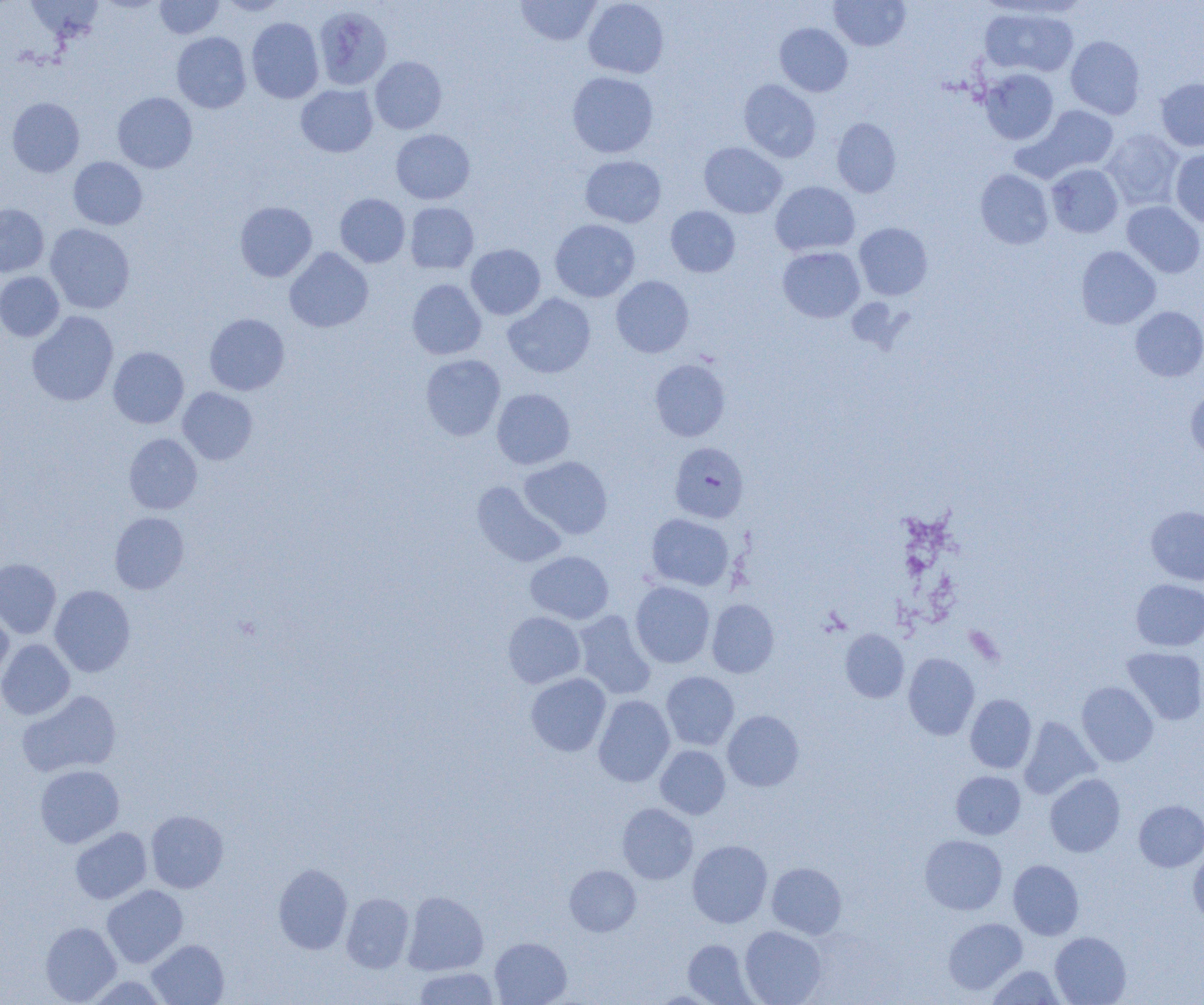
Summary:
  - Coordinate format: approximate bounding boxes as (x1,y1)-(x2,y2) corner pairs in pixels
  - Uninfected red blood cell locations: (26,0)-(103,43), (154,0)-(224,39), (218,0)-(289,16), (516,0)-(602,46), (583,0)-(669,78), (829,0)-(910,51), (314,6)-(392,91), (980,7)-(1079,77), (246,17)-(324,103), (775,23)-(853,96), (172,32)-(251,113), (1066,35)-(1145,119), (370,56)-(447,134), (980,69)-(1058,144), (567,72)-(658,158), (1155,77)-(1204,152), (739,80)-(821,162), (296,84)-(378,157), (112,92)-(197,173), (7,97)-(85,177), (1027,105)-(1119,177), (832,117)-(901,197), (391,129)-(475,204), (1102,129)-(1184,210), (698,142)-(786,218), (1170,149)-(1204,228), (580,155)-(666,227), (68,157)-(147,229), (1046,163)-(1123,238), (975,169)-(1053,249), (771,181)-(860,256), (335,193)-(410,267), (235,201)-(317,282), (1121,201)-(1204,278), (405,202)-(479,274), (0,203)-(49,277), (665,206)-(740,277), (550,219)-(640,302), (854,222)-(933,300), (45,224)-(135,314), (466,244)-(546,320), (1076,245)-(1161,330), (778,246)-(865,322), (284,247)-(373,332), (0,271)-(64,341), (611,275)-(694,357), (407,279)-(487,360), (503,293)-(596,378), (1130,306)-(1204,381), (26,311)-(119,406), (204,313)-(289,395), (108,346)-(189,428), (420,354)-(505,441), (650,359)-(730,441), (177,387)-(258,465), (492,388)-(575,469), (1185,389)-(1204,461), (124,433)-(202,514), (519,456)-(613,539), (471,481)-(567,567), (1146,505)-(1204,585), (109,512)-(189,594), (646,513)-(734,591), (525,551)-(614,624), (0,558)-(61,639), (1131,578)-(1204,651), (630,581)-(715,668), (49,585)-(136,676), (707,599)-(779,677), (0,608)-(13,686), (573,610)-(656,699), (503,611)-(585,688), (840,629)-(909,702), (0,639)-(75,719), (1121,647)-(1204,725), (903,653)-(979,739), (661,671)-(740,750), (526,673)-(611,756), (1076,681)-(1158,766), (18,689)-(122,777), (965,694)-(1037,773), (593,695)-(675,787), (722,710)-(804,791), (1019,717)-(1100,799), (655,745)-(730,819), (34,764)-(124,848), (951,771)-(1025,839), (1045,774)-(1125,857), (1134,799)-(1204,872), (617,803)-(698,884), (145,809)-(228,893), (70,827)-(152,904), (920,834)-(1007,914), (687,839)-(772,928), (1188,850)-(1204,925), (1008,859)-(1084,940), (766,862)-(846,939), (273,863)-(353,954), (565,865)-(641,936), (102,884)-(188,968), (403,891)-(488,975), (341,893)-(414,972), (943,918)-(1027,994), (40,921)-(121,1004), (740,925)-(827,1005), (1050,931)-(1131,1005), (490,937)-(572,1005), (146,939)-(229,1005), (683,939)-(756,1004), (986,965)-(1064,1004), (413,967)-(499,1004), (85,975)-(171,1005)
  - Plasmodium falciparum-infected red blood cell locations: (669,442)-(749,523)
  - Slide-level diagnosis: Plasmodium falciparum
  - Magnification: 1000x
  - Field of view: one of a larger specimen
  - Image size: 1204×1005 pixels
  - Modality: optical microscopy
  - Preparation: thin blood film